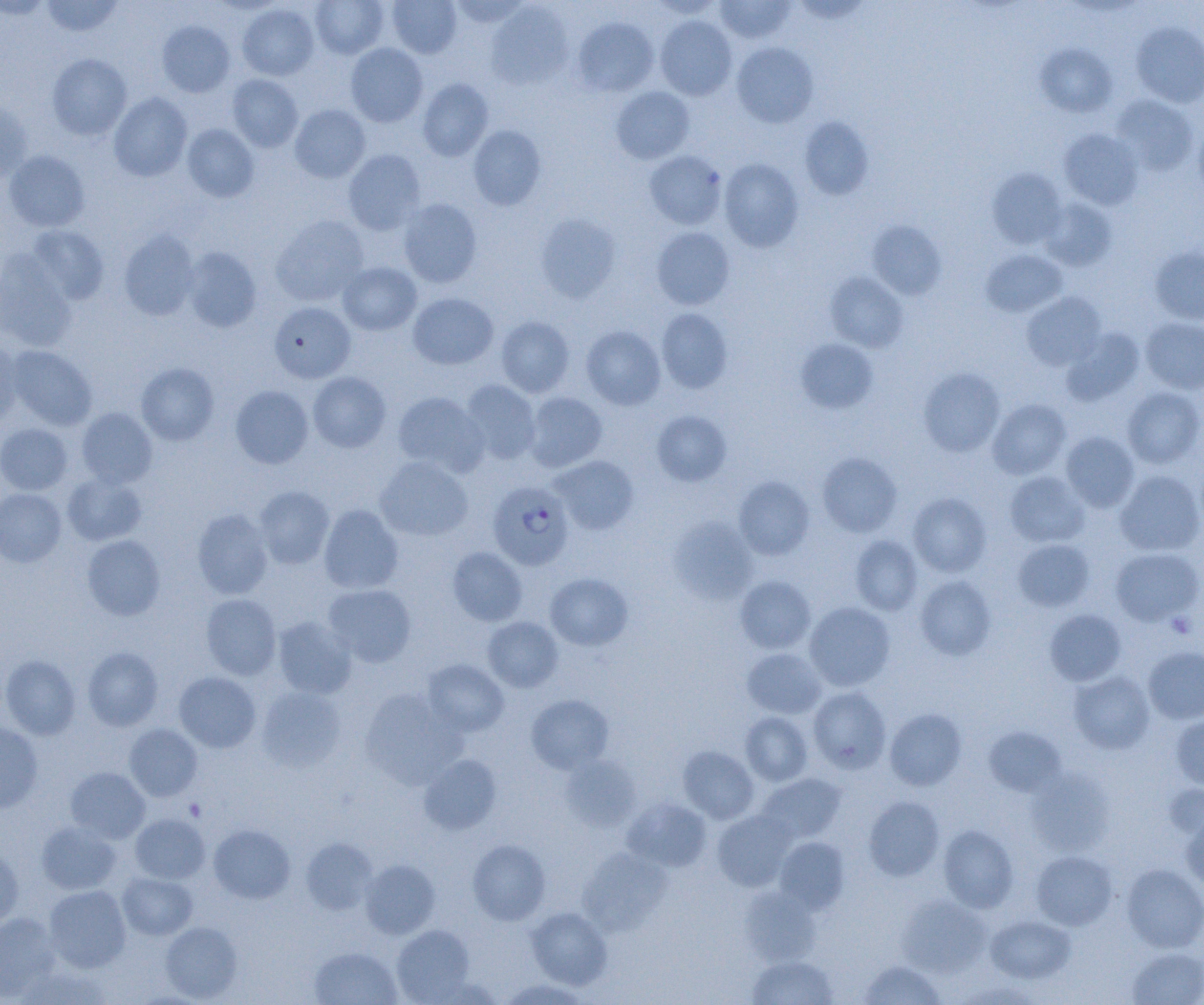

slide-level diagnosis = Plasmodium falciparum
modality = optical microscopy
uninfected red blood cell locations = approximate bounding boxes as (x1,y1)-(x2,y2) corner pairs in pixels: (0,0)-(53,19), (40,0)-(123,37), (310,0)-(389,59), (387,0)-(462,59), (448,0)-(531,27), (649,0)-(724,19), (715,0)-(796,44), (487,1)-(573,89), (237,4)-(319,80), (655,15)-(737,100), (572,17)-(659,97), (157,20)-(235,97), (1132,21)-(1204,107), (732,42)-(818,127), (345,43)-(428,127), (1036,44)-(1117,117), (47,53)-(132,140), (227,74)-(303,152), (417,78)-(493,161), (611,86)-(694,164), (109,92)-(192,182), (1111,95)-(1198,175), (0,98)-(32,181), (290,105)-(370,183), (800,117)-(874,200), (1194,122)-(1204,203), (182,124)-(259,203), (467,125)-(546,210), (1059,128)-(1144,210), (343,149)-(426,234), (3,150)-(90,232), (644,150)-(726,230), (719,158)-(804,251), (986,168)-(1067,249), (398,198)-(482,287), (1039,198)-(1117,271), (535,214)-(621,302), (270,215)-(369,306), (868,221)-(946,300), (26,224)-(109,305), (651,227)-(734,310), (119,229)-(199,321), (1149,246)-(1204,325), (181,247)-(261,332), (981,250)-(1067,317), (0,253)-(77,351), (337,262)-(421,335), (825,272)-(908,353), (1022,292)-(1106,370), (408,293)-(498,369), (269,301)-(356,383), (656,308)-(733,393), (496,316)-(575,397), (1140,317)-(1204,394), (581,325)-(666,410), (1061,328)-(1145,406), (0,337)-(23,426), (795,338)-(878,414), (6,345)-(97,430), (136,362)-(219,445), (918,367)-(1005,457), (308,371)-(391,452), (460,379)-(541,464), (230,385)-(313,468), (1122,387)-(1204,469), (392,392)-(488,476), (524,392)-(607,472), (987,399)-(1071,479), (77,408)-(157,488), (651,410)-(731,486), (0,423)-(73,495), (1060,432)-(1139,512), (817,452)-(902,537), (375,456)-(473,542), (551,456)-(638,534), (1115,470)-(1204,556), (1004,471)-(1089,547), (63,472)-(147,546), (734,476)-(815,560), (254,485)-(335,569), (0,488)-(66,567), (907,493)-(992,577), (319,504)-(403,594), (191,508)-(274,599), (669,517)-(758,604), (82,535)-(165,620), (850,535)-(922,616), (1013,539)-(1094,612), (447,547)-(527,626), (1110,547)-(1203,626), (544,572)-(633,650), (735,575)-(816,654), (914,575)-(997,660), (323,584)-(417,667), (201,594)-(282,680), (804,601)-(895,691), (1044,609)-(1126,686), (273,616)-(357,699), (483,616)-(563,692), (1143,646)-(1204,724), (82,647)-(163,731), (742,648)-(827,719), (1,654)-(81,739), (422,659)-(509,736), (1068,670)-(1155,754), (174,671)-(261,753), (257,686)-(347,773), (808,687)-(892,774), (360,688)-(467,789), (526,694)-(614,773), (885,708)-(967,790), (740,711)-(813,786), (1170,713)-(1204,790), (0,721)-(43,814), (124,723)-(202,801), (984,726)-(1066,797), (678,745)-(759,823), (419,753)-(502,835), (559,755)-(641,831), (65,767)-(150,843), (1026,767)-(1115,856), (756,773)-(846,845), (1164,781)-(1204,840), (863,796)-(945,881), (622,797)-(712,871), (712,810)-(795,891), (1181,812)-(1204,890), (130,814)-(209,883), (36,821)-(122,895), (209,824)-(295,904), (938,825)-(1019,912), (774,836)-(849,913), (301,837)-(377,914), (468,838)-(550,925), (0,843)-(23,930), (578,847)-(672,934), (1031,850)-(1117,930), (360,859)-(440,939), (1122,864)-(1204,952), (117,872)-(198,940), (44,885)-(131,972), (740,886)-(819,966), (897,895)-(991,977), (526,907)-(612,989), (0,913)-(61,1002), (986,915)-(1076,984), (160,921)-(243,1002), (392,924)-(475,1004), (1126,946)-(1204,1005), (310,947)-(401,1005), (747,955)-(839,1004), (859,958)-(945,1004), (498,978)-(591,1005)
preparation = thin blood film
platelet locations = approximate bounding boxes as (x1,y1)-(x2,y2) corner pairs in pixels: (1167,612)-(1197,638), (184,798)-(206,820)
image size = 1204×1005 pixels
magnification = 1000x
field of view = single
Plasmodium falciparum-infected red blood cell locations = approximate bounding boxes as (x1,y1)-(x2,y2) corner pairs in pixels: (488,480)-(574,570)